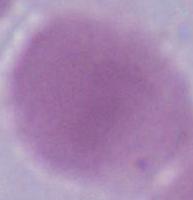
An erythrocyte is seen. Captured at 1000x magnification. Photomicrograph.